State the blood parasite species.
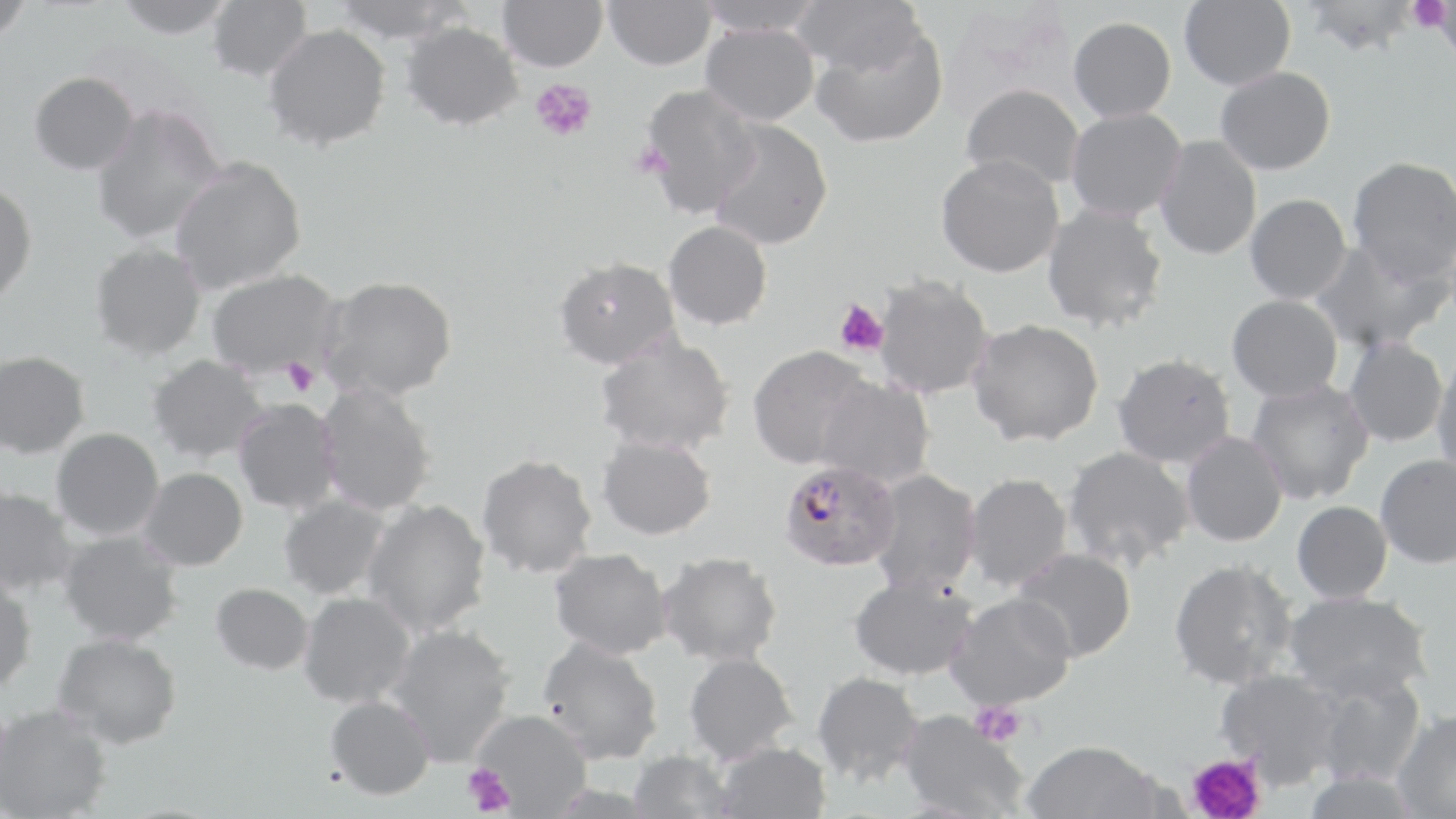
Plasmodium falciparum.

Summary:
  - Coordinate format: approximate bounding boxes as (x1, y1, x2, y2) in pixels
  - Platelet locations: (1409, 0, 1452, 35), (530, 78, 597, 142), (835, 299, 888, 357), (281, 357, 319, 396), (971, 702, 1026, 747), (1187, 753, 1266, 819), (463, 764, 516, 816)
  - Plasmodium falciparum-infected red blood cell locations: (779, 460, 900, 572)
  - Uninfected red blood cell locations: (0, 0, 35, 46), (112, 0, 238, 41), (207, 0, 312, 82), (330, 0, 472, 44), (498, 0, 607, 72), (604, 0, 716, 70), (694, 0, 826, 37), (791, 0, 925, 78), (1179, 0, 1296, 89), (1302, 0, 1420, 56), (1069, 16, 1177, 122), (400, 20, 524, 130), (701, 21, 820, 125), (263, 24, 392, 151), (810, 24, 948, 149), (1216, 66, 1336, 175), (29, 73, 139, 176), (638, 83, 763, 220), (961, 83, 1084, 191), (90, 104, 228, 246), (1066, 107, 1187, 223), (707, 119, 833, 250), (1154, 134, 1262, 260), (935, 154, 1065, 277), (1347, 155, 1456, 285), (170, 158, 307, 294), (0, 181, 37, 307), (1245, 193, 1352, 304), (1041, 203, 1169, 333), (663, 220, 772, 330), (1308, 238, 1453, 354), (90, 242, 207, 360), (554, 256, 680, 370), (207, 268, 342, 380), (871, 274, 994, 399), (319, 275, 457, 402), (1227, 294, 1343, 402), (968, 318, 1104, 447), (596, 331, 735, 456), (1344, 336, 1448, 447), (748, 345, 874, 470), (0, 350, 91, 458), (1431, 352, 1456, 482), (1112, 353, 1236, 469), (148, 354, 270, 463), (814, 375, 935, 488), (1247, 378, 1375, 505), (316, 383, 437, 516), (233, 399, 341, 515), (50, 427, 165, 540), (1181, 430, 1288, 547), (597, 434, 716, 540), (1061, 445, 1195, 570), (476, 453, 598, 578), (1375, 454, 1456, 569), (138, 467, 248, 571), (866, 468, 983, 596), (963, 472, 1073, 592), (0, 485, 78, 597), (278, 493, 392, 601), (362, 498, 492, 637), (1291, 500, 1392, 603), (58, 529, 184, 646), (549, 547, 673, 659), (1012, 547, 1136, 662), (658, 551, 783, 666), (1168, 557, 1297, 689), (847, 572, 979, 680), (0, 574, 37, 694), (211, 582, 314, 675), (298, 591, 416, 708), (946, 591, 1077, 710), (1283, 591, 1432, 702), (383, 624, 516, 766), (52, 633, 182, 749), (537, 635, 664, 764), (684, 652, 799, 764), (1216, 667, 1344, 786), (812, 671, 924, 786), (1309, 675, 1427, 787), (325, 695, 435, 800), (0, 704, 112, 819), (469, 709, 592, 816), (1390, 709, 1456, 818), (898, 710, 1029, 819), (1021, 739, 1162, 819), (713, 741, 830, 819), (626, 749, 735, 819)
  - Image size: 1456×819 pixels
  - Modality: light microscopy
  - Preparation: thin blood smear
  - Field of view: one of a larger specimen
  - Stain: May-Grünwald-Giemsa
  - Magnification: 1000x